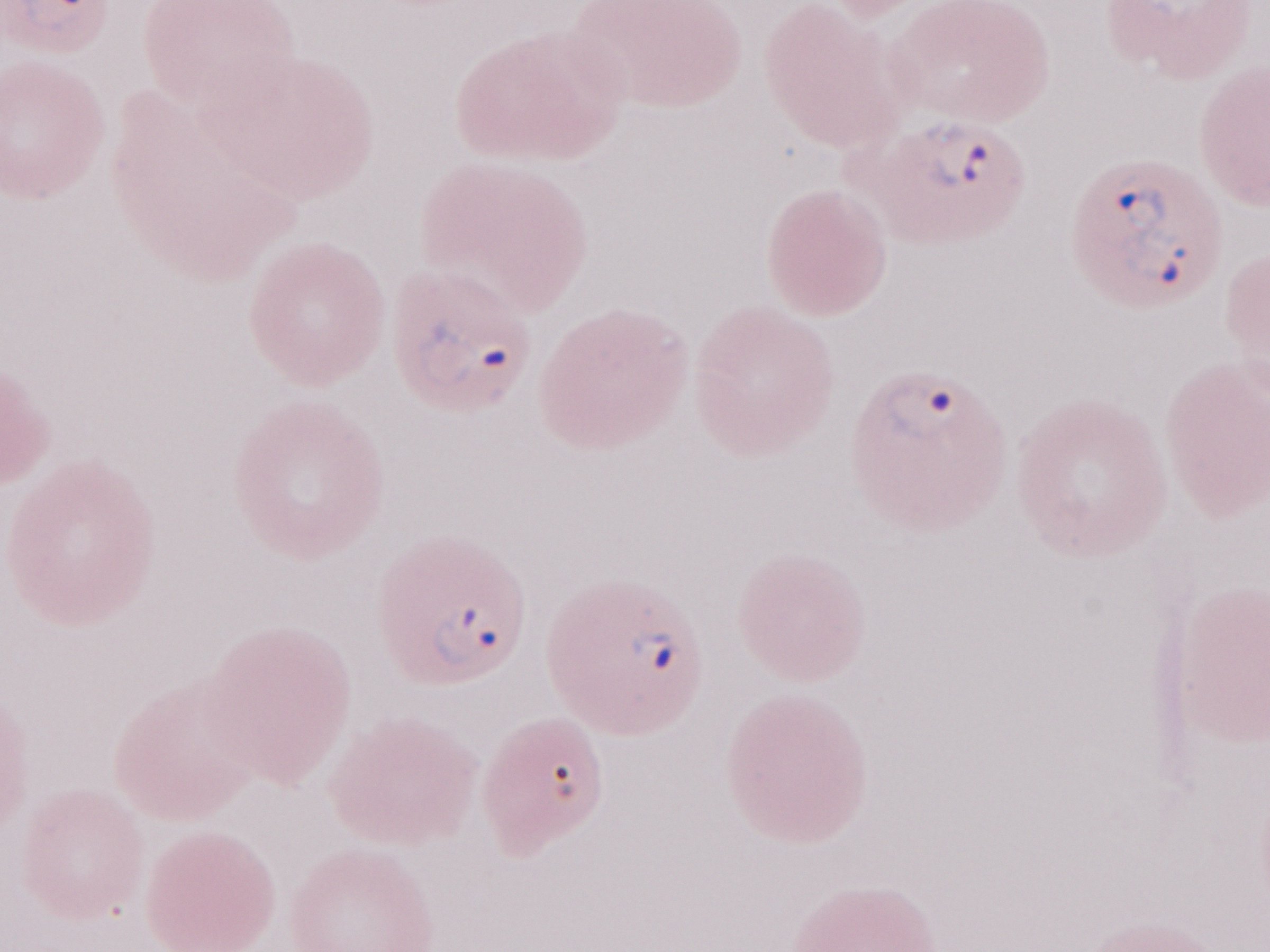

Patient diagnosis: malaria infection. Magnification: 1,000x. May-Grünwald-Giemsa stain. Olympus BX43 microscope, Olympus DP73 camera. Thin peripheral-blood smear. Image is 1270×952 pixels. One field of this slide.